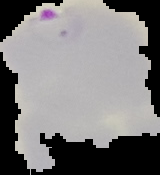

image type = segmented cell region on a black background
preparation = thin blood smear
malaria status = parasitized
image size = 160×175 pixels